Name the parasite shown.
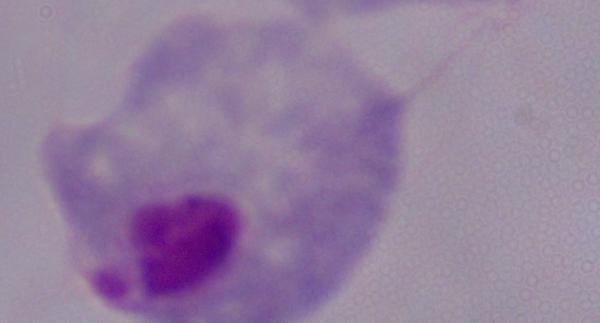
A trichomonad.

Captured at 1000x magnification. Micrograph.